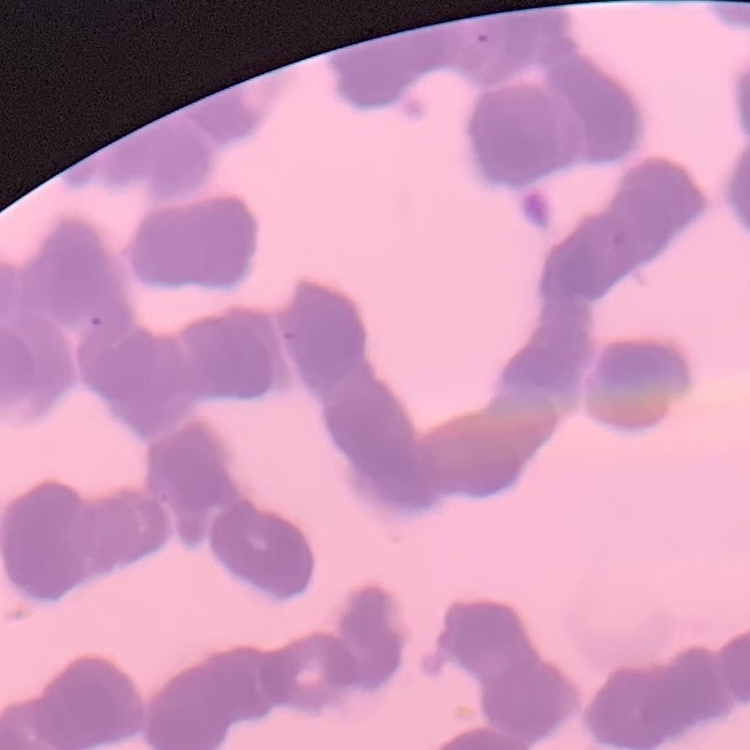
red blood cell morphology = rouleaux formation
preparation = thin peripheral smear
stain = Field's or Giemsa
image type = one tile cut from a larger photomicrograph